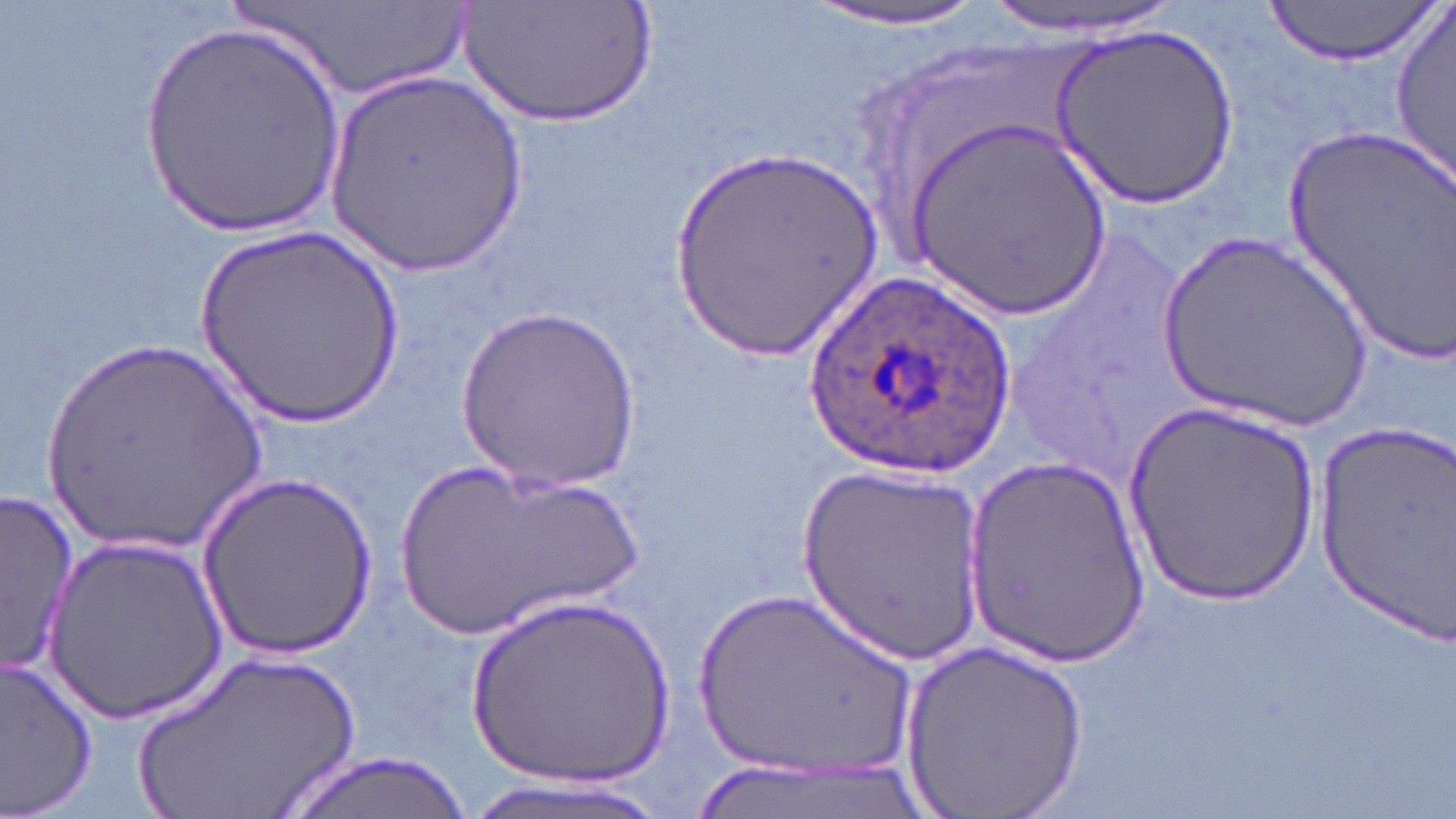

Summary:
  - Coordinate format: approximate bounding boxes as named x1/y1/x2/y2 corners in pixels
  - Plasmodium ovale-infected red blood cell locations: (x1=801, y1=268, x2=1023, y2=485)
  - Uninfected red blood cell locations: (x1=460, y1=0, x2=660, y2=127), (x1=978, y1=0, x2=1190, y2=37), (x1=1261, y1=0, x2=1442, y2=66), (x1=231, y1=2, x2=482, y2=99), (x1=796, y1=2, x2=1003, y2=34), (x1=1388, y1=4, x2=1455, y2=195), (x1=1052, y1=22, x2=1240, y2=206), (x1=138, y1=23, x2=347, y2=243), (x1=320, y1=68, x2=528, y2=279), (x1=903, y1=113, x2=1115, y2=319), (x1=1285, y1=121, x2=1453, y2=364), (x1=668, y1=147, x2=887, y2=360), (x1=195, y1=221, x2=410, y2=428), (x1=1153, y1=230, x2=1376, y2=432), (x1=457, y1=302, x2=639, y2=492), (x1=34, y1=334, x2=277, y2=560), (x1=1124, y1=401, x2=1319, y2=605), (x1=1313, y1=421, x2=1454, y2=640), (x1=959, y1=453, x2=1151, y2=664), (x1=391, y1=456, x2=646, y2=643), (x1=795, y1=463, x2=988, y2=665), (x1=198, y1=476, x2=380, y2=657), (x1=0, y1=490, x2=80, y2=678), (x1=45, y1=536, x2=229, y2=723), (x1=683, y1=582, x2=925, y2=786), (x1=465, y1=590, x2=677, y2=790), (x1=901, y1=639, x2=1096, y2=818), (x1=124, y1=645, x2=368, y2=819), (x1=0, y1=653, x2=100, y2=819), (x1=281, y1=752, x2=472, y2=819), (x1=453, y1=772, x2=682, y2=819)
  - Slide-level diagnosis: Plasmodium ovale
  - Preparation: thin blood smear
  - Field of view: single
  - Magnification: 1000x
  - Stain: May-Grünwald-Giemsa
  - Modality: light microscopy
  - Image size: 1456×819 pixels